Assess for malaria.
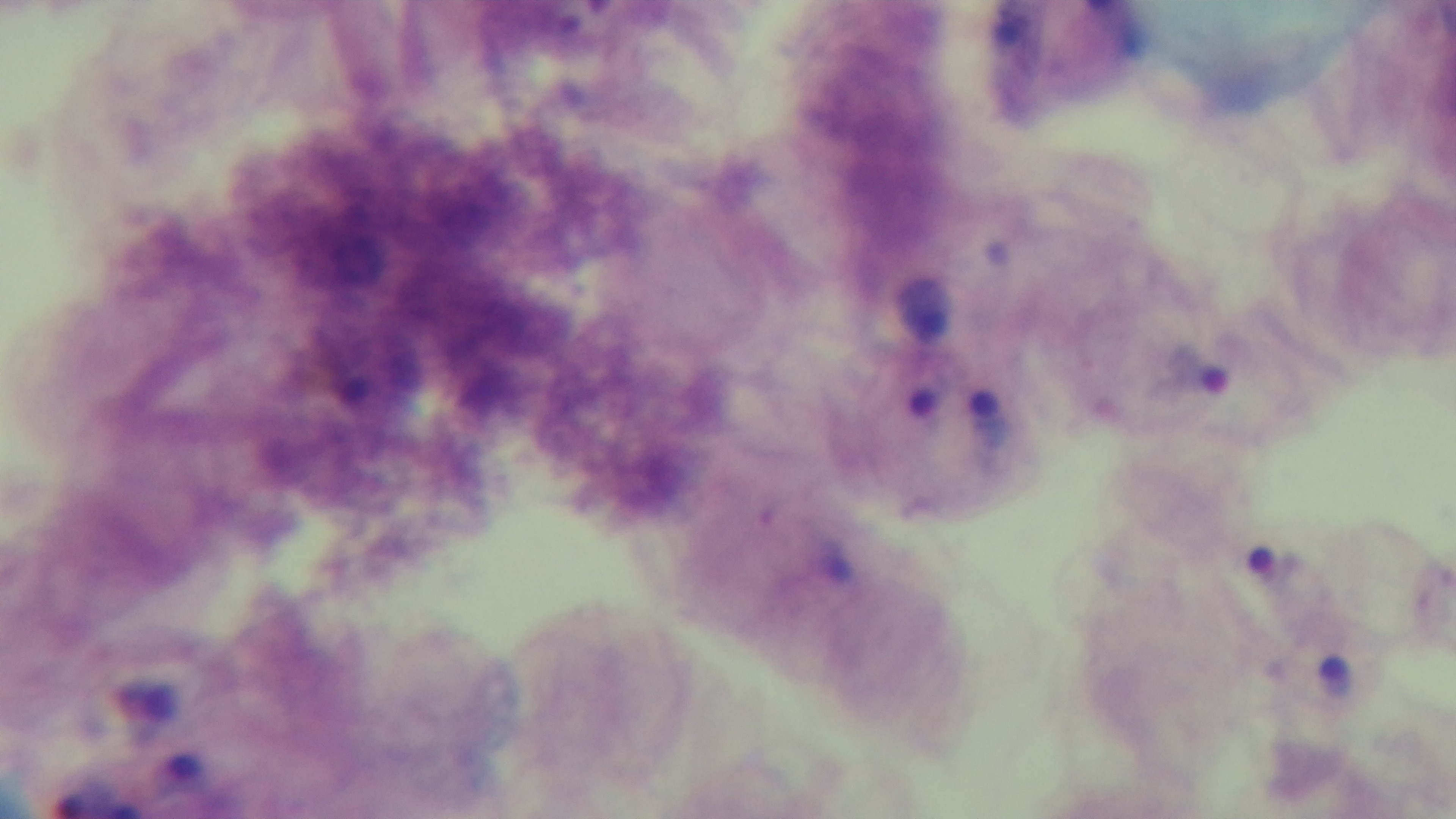
It is infected.

Photomicrograph. 100x oil-immersion objective. Mounted 4K digital camera. Single field of view. Preparation: thick. Giemsa stain.